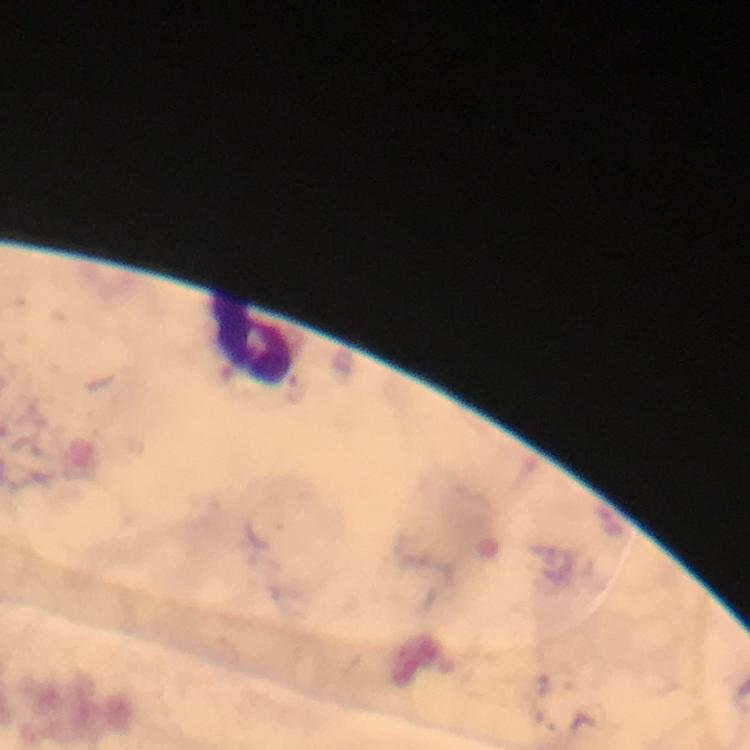

capture: smartphone mounted on the microscope
leukocyte_locations: 'approximate centers as [x, y] in pixels: [247, 339]'
stain: Giemsa
cropped_from: a single field of view
plasmodium_parasites: none seen
preparation: thick smear
image_size: 750×750 pixels
magnification: 100x
immersion_oil: applied
context: from a malaria diagnostic workup